State which parasite is depicted.
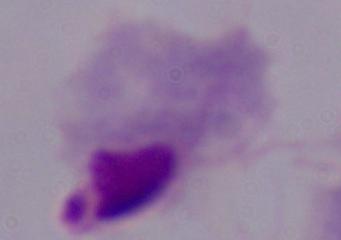

A trichomonad.

Micrograph. Captured at 1000x magnification.